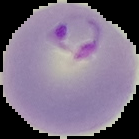
Summary:
  - Image size: 139×139 pixels
  - Preparation: thin blood smear
  - Malaria status: parasitized
  - Image type: segmented cell region on a black background